Locate every uninfected red blood cell.
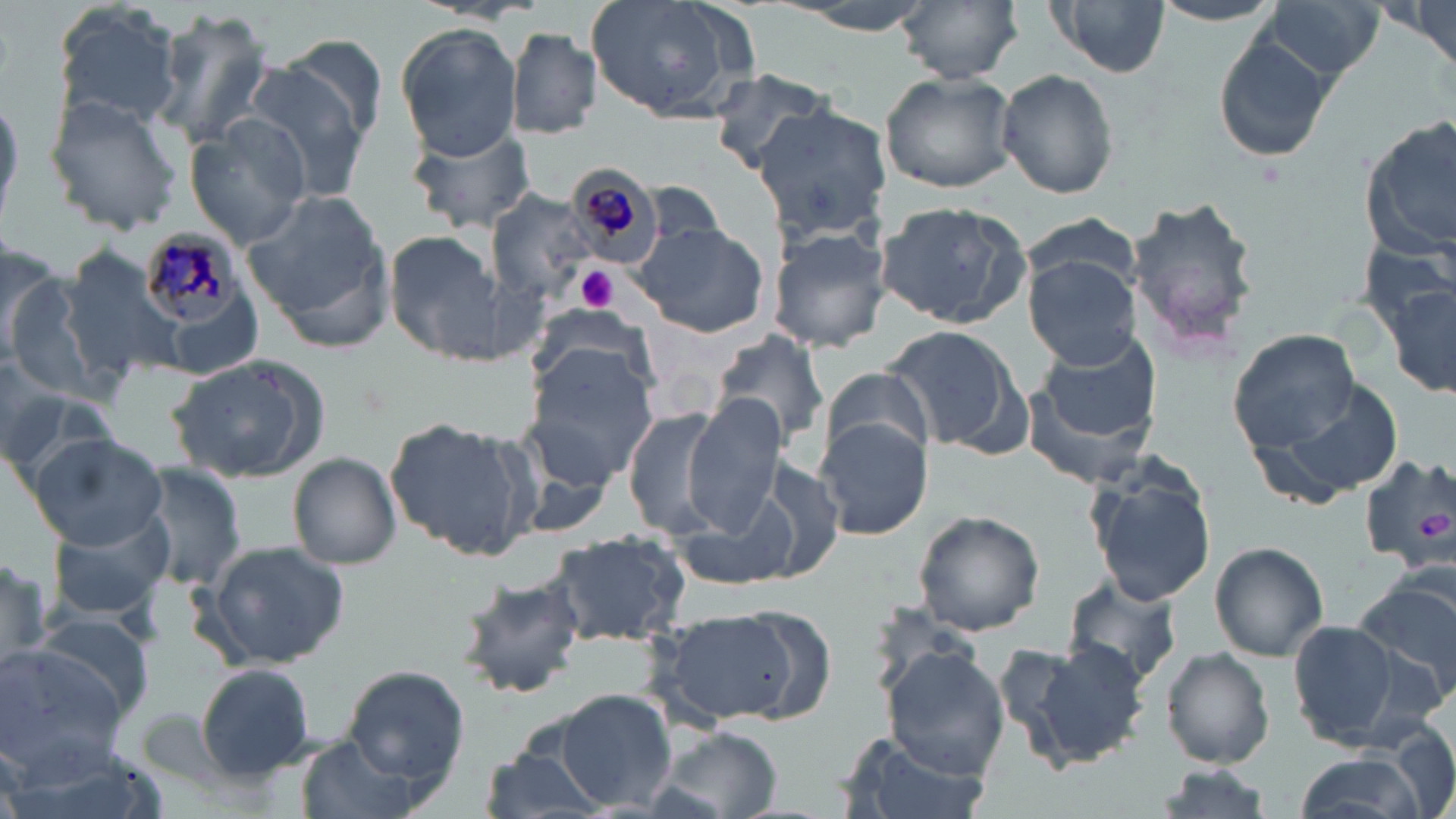

Approximate bounding boxes as (x1, y1, x2, y2) in pixels.
Uninfected red blood cells: (895, 0, 1023, 85), (1047, 0, 1170, 81), (1145, 0, 1286, 27), (587, 1, 758, 123), (771, 1, 939, 34), (1256, 1, 1386, 85), (1394, 1, 1456, 72), (49, 3, 183, 135), (150, 12, 275, 149), (1210, 26, 1336, 167), (395, 27, 522, 160), (506, 27, 602, 139), (283, 38, 390, 141), (702, 67, 836, 168), (238, 69, 371, 202), (996, 69, 1119, 198), (880, 72, 1019, 194), (0, 89, 23, 230), (44, 95, 183, 237), (754, 103, 893, 246), (1358, 114, 1456, 262), (183, 119, 312, 246), (407, 123, 537, 234), (244, 188, 393, 345), (487, 191, 598, 304), (1126, 196, 1264, 355), (874, 202, 1032, 328), (1021, 212, 1139, 297), (633, 220, 770, 339), (765, 224, 891, 354), (385, 231, 506, 361), (59, 247, 191, 384), (1023, 253, 1142, 369), (2, 262, 100, 395), (1381, 276, 1456, 402), (525, 303, 659, 404), (877, 323, 1028, 455), (1228, 329, 1362, 452), (1037, 330, 1164, 450), (709, 331, 832, 456), (522, 345, 661, 488), (0, 349, 64, 461), (167, 353, 332, 482), (820, 370, 937, 462), (1252, 372, 1407, 509), (0, 373, 112, 489), (679, 395, 789, 538), (622, 407, 734, 540), (382, 415, 536, 561), (815, 418, 933, 541), (30, 432, 167, 550), (1079, 451, 1220, 611), (288, 453, 402, 569), (1357, 453, 1456, 571), (133, 464, 245, 593), (677, 488, 802, 592), (46, 507, 176, 624), (912, 509, 1045, 636), (543, 532, 693, 647), (206, 541, 349, 669), (1210, 541, 1328, 660), (0, 551, 52, 679), (455, 567, 589, 701), (1349, 573, 1456, 710), (1061, 578, 1183, 691), (650, 610, 811, 725), (29, 612, 154, 724), (1285, 621, 1426, 750), (1007, 636, 1151, 768), (0, 644, 129, 779), (882, 647, 1010, 778), (1162, 648, 1275, 768), (196, 662, 316, 780), (342, 665, 469, 789), (555, 689, 678, 810), (646, 725, 783, 819), (840, 734, 989, 819), (294, 735, 425, 819), (475, 742, 611, 819), (1288, 749, 1431, 819), (1148, 765, 1278, 818).

Platelet locations: (575, 266, 618, 311). Plasmodium malariae-infected red blood cell locations: (563, 160, 670, 271), (139, 227, 260, 330). Slide-level diagnosis: Plasmodium malariae. Light microscopy. May-Grünwald-Giemsa stain. Thin blood smear. Captured at 1000x magnification. Image is 1456×819 pixels. Single field of view.